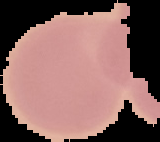

preparation = thin blood smear
image size = 160×142 pixels
malaria status = uninfected
image type = cell region segmented out of the field of view; surrounding area masked to black